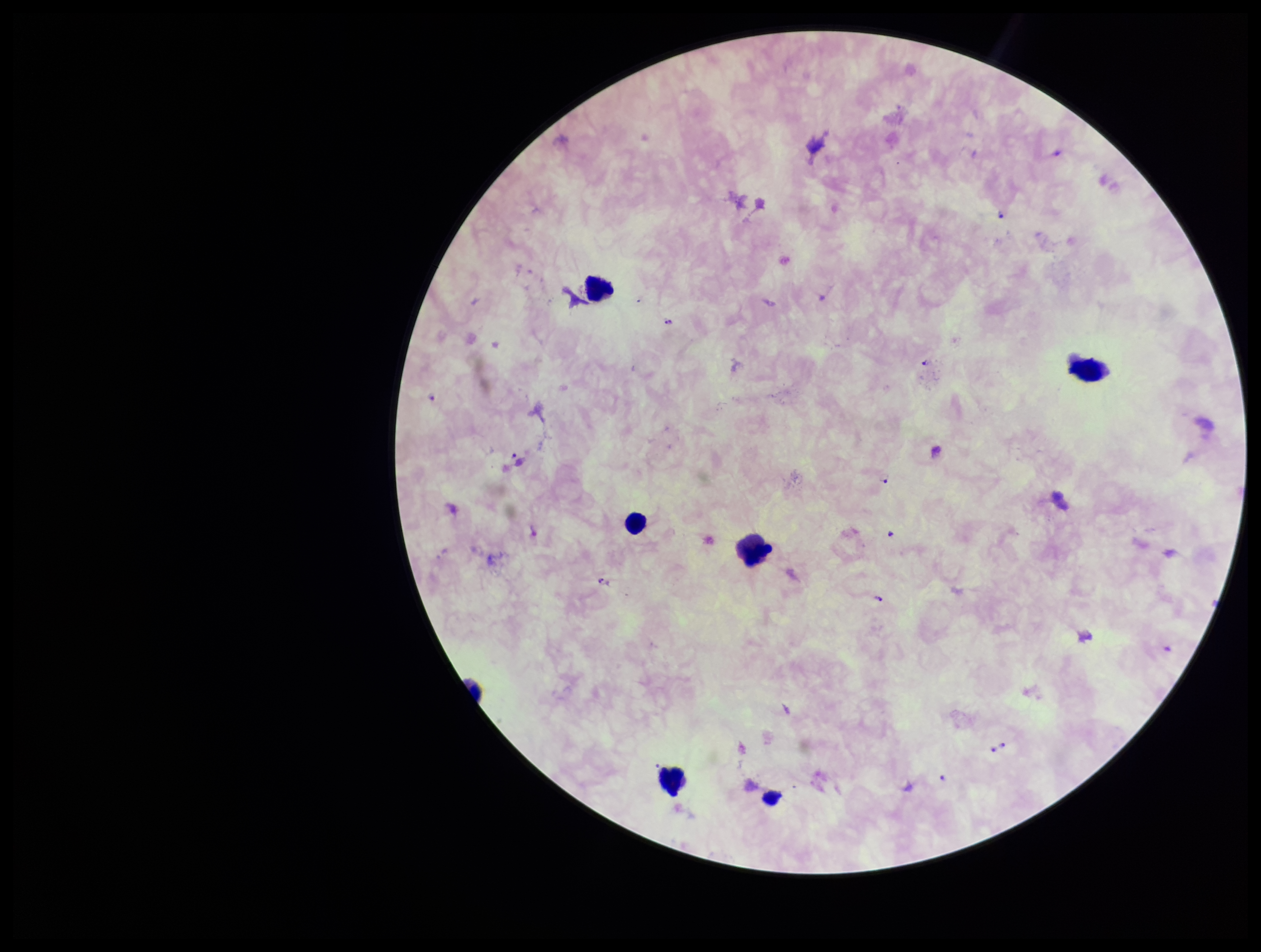
Summary:
  - Stain: Giemsa
  - Plasmodium parasites: detected
  - Parasite count: 12
  - Field of view: single
  - Preparation: thick
  - Patient malaria status: infected
  - Leukocyte count: 5
  - Image size: 1261×952 pixels
  - Species reported for this patient: Plasmodium falciparum
  - Capture: smartphone photograph through the microscope eyepiece